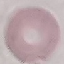
malaria_status: uninfected
image_type: cell patch, automatically extracted from a larger field of view and resized to 64 × 64 pixels
preparation: thin blood film
stain: Giemsa
capture: smartphone camera at the microscope eyepiece